Locate and identify every blood parasite.
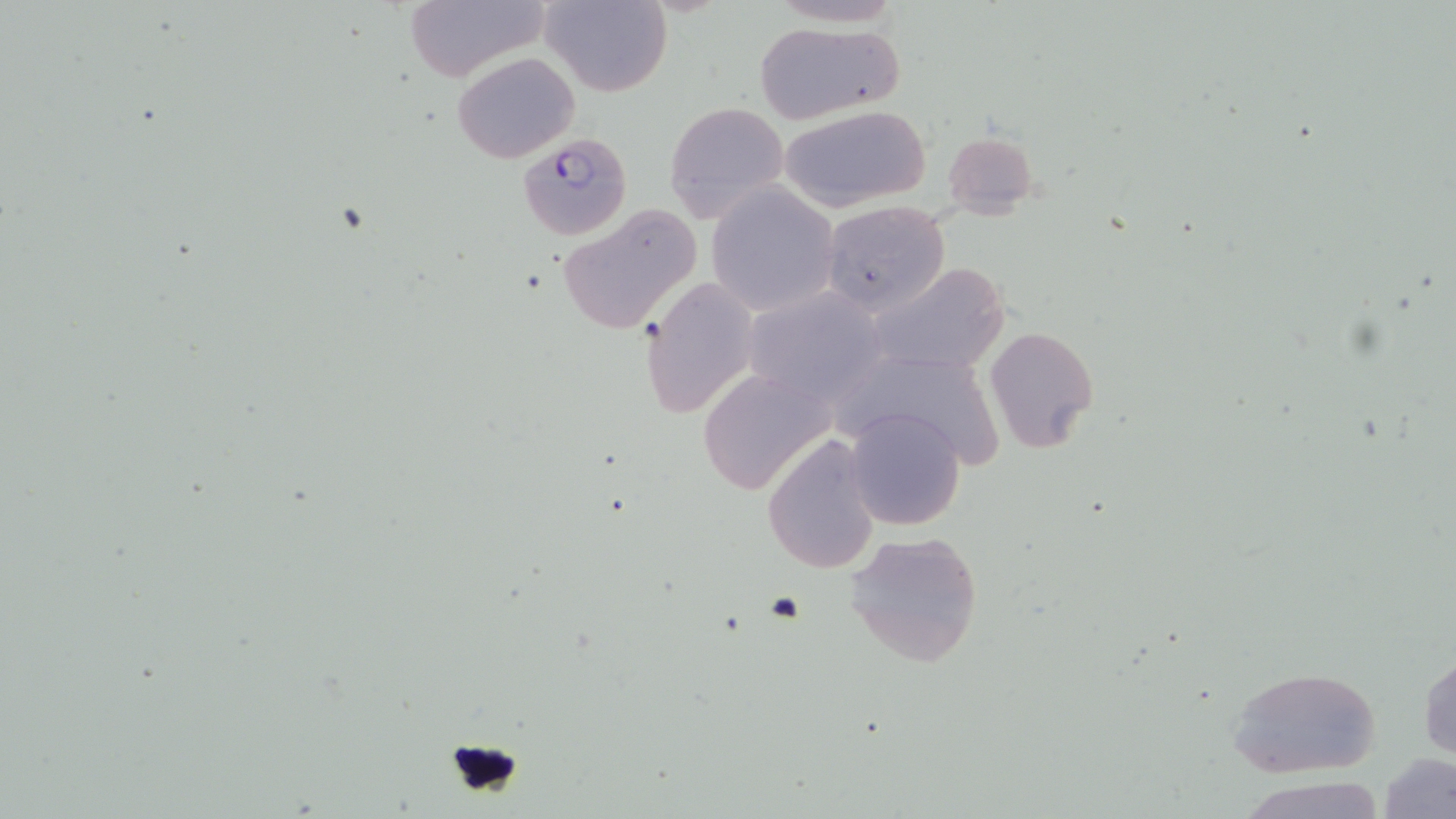
Approximate bounding boxes as named x1/y1/x2/y2 corners in pixels.
Plasmodium falciparum-infected red blood cells: (x1=517, y1=135, x2=630, y2=237).
No Plasmodium ovale, Plasmodium malariae, Plasmodium vivax, Babesia divergens, or Trypanosoma brucei observed.

Summary:
  - Uninfected red blood cell locations: (x1=402, y1=0, x2=548, y2=81), (x1=542, y1=0, x2=672, y2=98), (x1=752, y1=19, x2=905, y2=126), (x1=451, y1=51, x2=580, y2=163), (x1=663, y1=101, x2=790, y2=226), (x1=779, y1=104, x2=932, y2=211), (x1=941, y1=130, x2=1039, y2=218), (x1=705, y1=182, x2=841, y2=316), (x1=820, y1=201, x2=950, y2=318), (x1=555, y1=203, x2=704, y2=336), (x1=865, y1=261, x2=1012, y2=378), (x1=639, y1=278, x2=760, y2=419), (x1=742, y1=287, x2=889, y2=407), (x1=984, y1=324, x2=1100, y2=455), (x1=847, y1=363, x2=1003, y2=477), (x1=697, y1=367, x2=837, y2=495), (x1=842, y1=405, x2=968, y2=532), (x1=761, y1=434, x2=881, y2=576), (x1=842, y1=530, x2=987, y2=670), (x1=1419, y1=650, x2=1455, y2=762), (x1=1226, y1=665, x2=1382, y2=779), (x1=1377, y1=752, x2=1454, y2=819), (x1=1240, y1=773, x2=1389, y2=819)
  - Platelet locations: (x1=443, y1=736, x2=526, y2=801)
  - Slide-level diagnosis: Plasmodium falciparum
  - Magnification: 1000x
  - Image size: 1456×819 pixels
  - Field of view: single
  - Modality: light microscopy
  - Stain: May-Grünwald-Giemsa
  - Preparation: thin blood film